Report the malaria status of this cell.
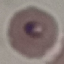

Parasitized.

Giemsa stain. Cell patch, automatically extracted from a larger field of view and resized to 64 × 64 pixels. Photographed with a smartphone camera at the microscope eyepiece. Thin blood smear.